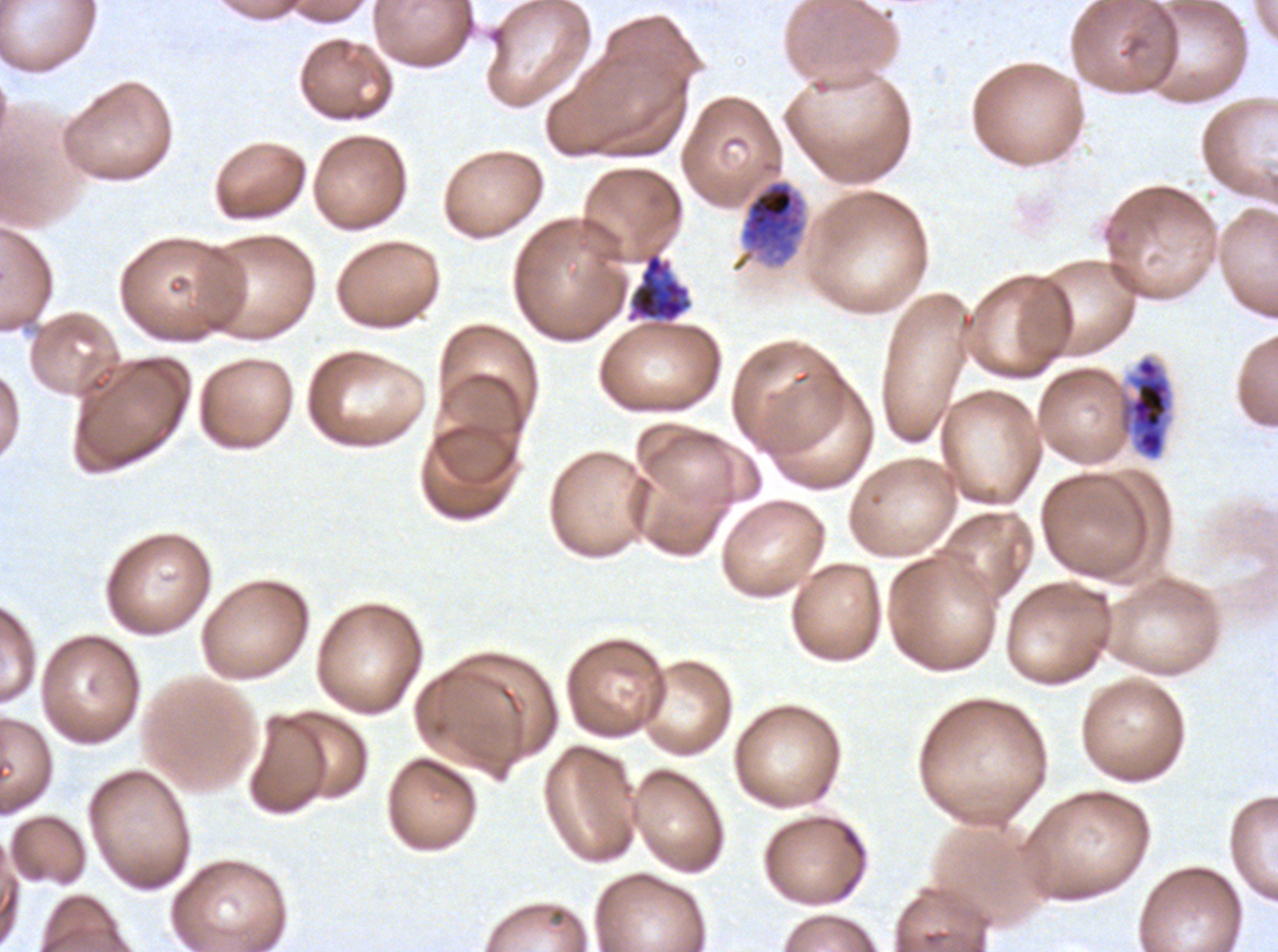

Approximate bounding boxes as {x1, y1, x2, y2} in pixels. Late trophozoite locations: {731, 178, 806, 272}. Segmenter locations: {627, 252, 693, 323}. Early schizont locations: {1121, 356, 1172, 459}. Giemsa stain. Life-cycle stages observed: late trophozoite, early schizont, segmenter. Ex-vivo Plasmodium falciparum culture from a patient in The Gambia, grown for 24 to 48 hours. Thin blood film. One sub-image of a larger composite. Image is 1278×952 pixels.